Assess this cell for malaria.
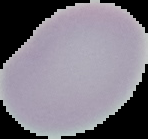

It is uninfected.

preparation = thin blood smear
image size = 148×139 pixels
image type = segmented cell region with the area outside set to black